Locate every blood parasite and identify its species.
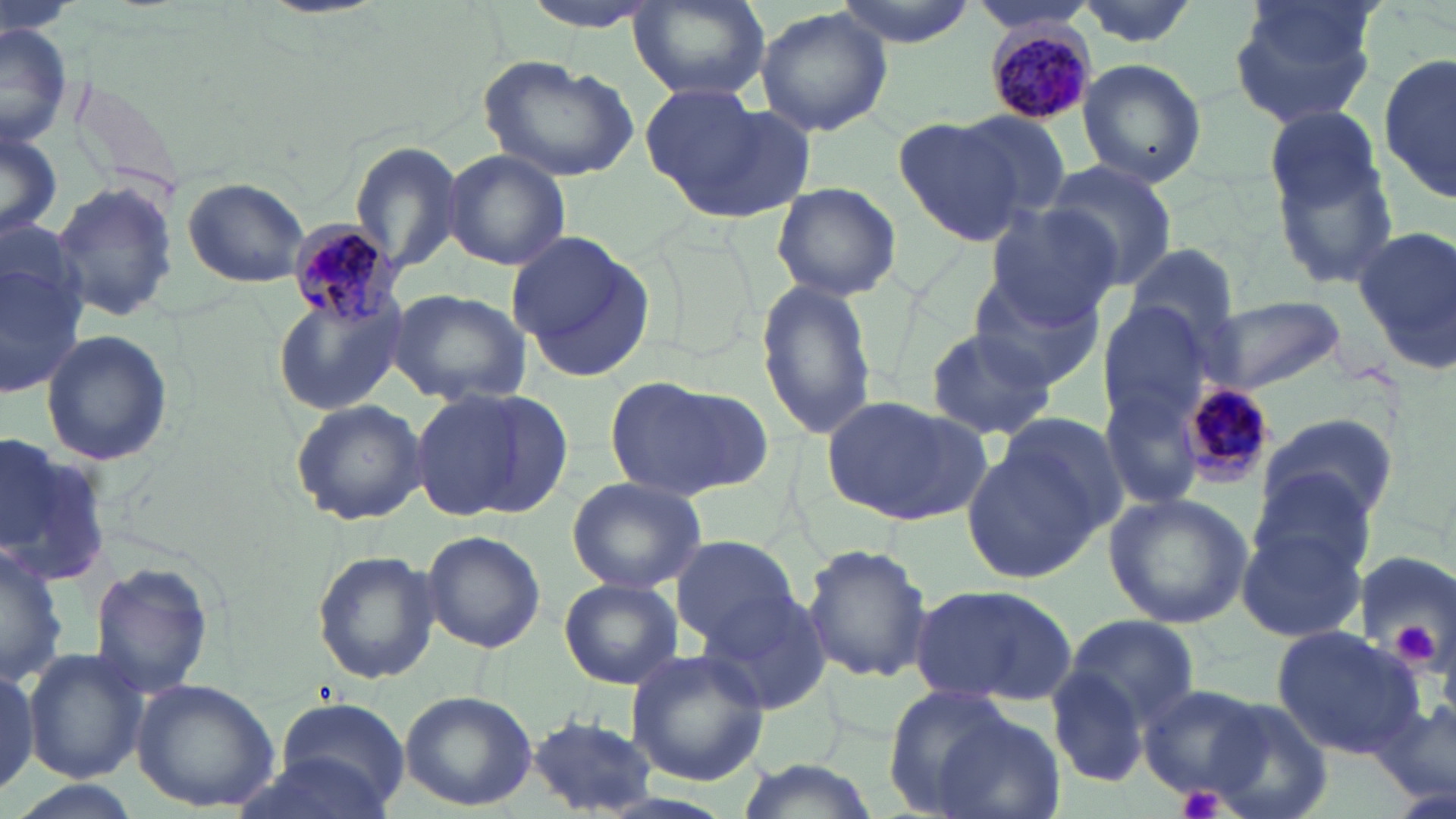
Approximate bounding boxes as (x1, y1, x2, y2) in pixels.
Plasmodium malariae-infected red blood cells: (982, 19, 1101, 129), (286, 218, 402, 330), (1183, 381, 1273, 478).
No Plasmodium falciparum, Plasmodium ovale, Plasmodium vivax, Babesia divergens, or Trypanosoma brucei observed.

Summary:
  - Platelet locations: (1392, 623, 1439, 664), (1180, 786, 1226, 819)
  - Uninfected red blood cell locations: (522, 0, 665, 33), (830, 0, 979, 47), (966, 0, 1101, 35), (629, 1, 769, 102), (1071, 1, 1205, 48), (1228, 1, 1380, 130), (754, 6, 894, 139), (0, 23, 72, 151), (1380, 54, 1455, 204), (475, 55, 641, 182), (1076, 58, 1207, 187), (641, 85, 807, 220), (1264, 104, 1383, 209), (953, 111, 1073, 216), (894, 116, 1025, 245), (0, 128, 62, 241), (1268, 133, 1401, 290), (351, 142, 466, 275), (442, 149, 571, 272), (1044, 159, 1178, 294), (183, 175, 310, 288), (47, 180, 181, 324), (771, 181, 902, 300), (982, 207, 1123, 327), (1353, 224, 1456, 367), (0, 228, 93, 402), (505, 230, 659, 383), (1123, 242, 1239, 349), (970, 277, 1101, 390), (755, 281, 877, 439), (387, 289, 532, 407), (275, 291, 404, 416), (1203, 296, 1346, 392), (1096, 301, 1216, 429), (922, 328, 1061, 442), (41, 329, 171, 466), (603, 374, 768, 503), (1100, 379, 1210, 513), (413, 386, 570, 525), (821, 395, 988, 527), (290, 397, 427, 526), (995, 408, 1130, 538), (1256, 412, 1397, 532), (961, 431, 1113, 584), (0, 440, 115, 589), (1248, 469, 1381, 584), (564, 476, 709, 593), (1102, 491, 1254, 628), (1236, 522, 1369, 643), (420, 531, 547, 653), (669, 534, 802, 649), (802, 543, 934, 686), (310, 548, 442, 686), (1350, 550, 1455, 677), (90, 559, 215, 697), (558, 579, 683, 691), (909, 582, 1080, 706), (696, 585, 836, 717), (1062, 614, 1202, 726), (1270, 627, 1431, 761), (23, 648, 149, 783), (624, 649, 770, 786), (0, 661, 42, 796), (1045, 663, 1156, 790), (131, 678, 280, 812), (1136, 682, 1278, 804), (882, 683, 1020, 813), (397, 689, 537, 811), (273, 695, 410, 813), (1197, 699, 1333, 819), (927, 712, 1065, 819), (526, 713, 658, 811), (229, 749, 398, 818), (732, 757, 883, 819), (3, 777, 143, 819)
  - Slide-level diagnosis: Plasmodium malariae
  - Preparation: thin blood film
  - Modality: light microscopy
  - Image size: 1456×819 pixels
  - Stain: May-Grünwald-Giemsa
  - Magnification: 1000x
  - Field of view: single